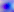 Captured at 400x magnification. Micrograph. Toxoplasma gondii is shown.